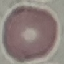
result = negative for malaria parasites
stain = Giemsa
image type = cell patch, automatically extracted from a larger field of view and resized to 64 × 64 pixels
preparation = thin blood film
capture = smartphone through the microscope eyepiece